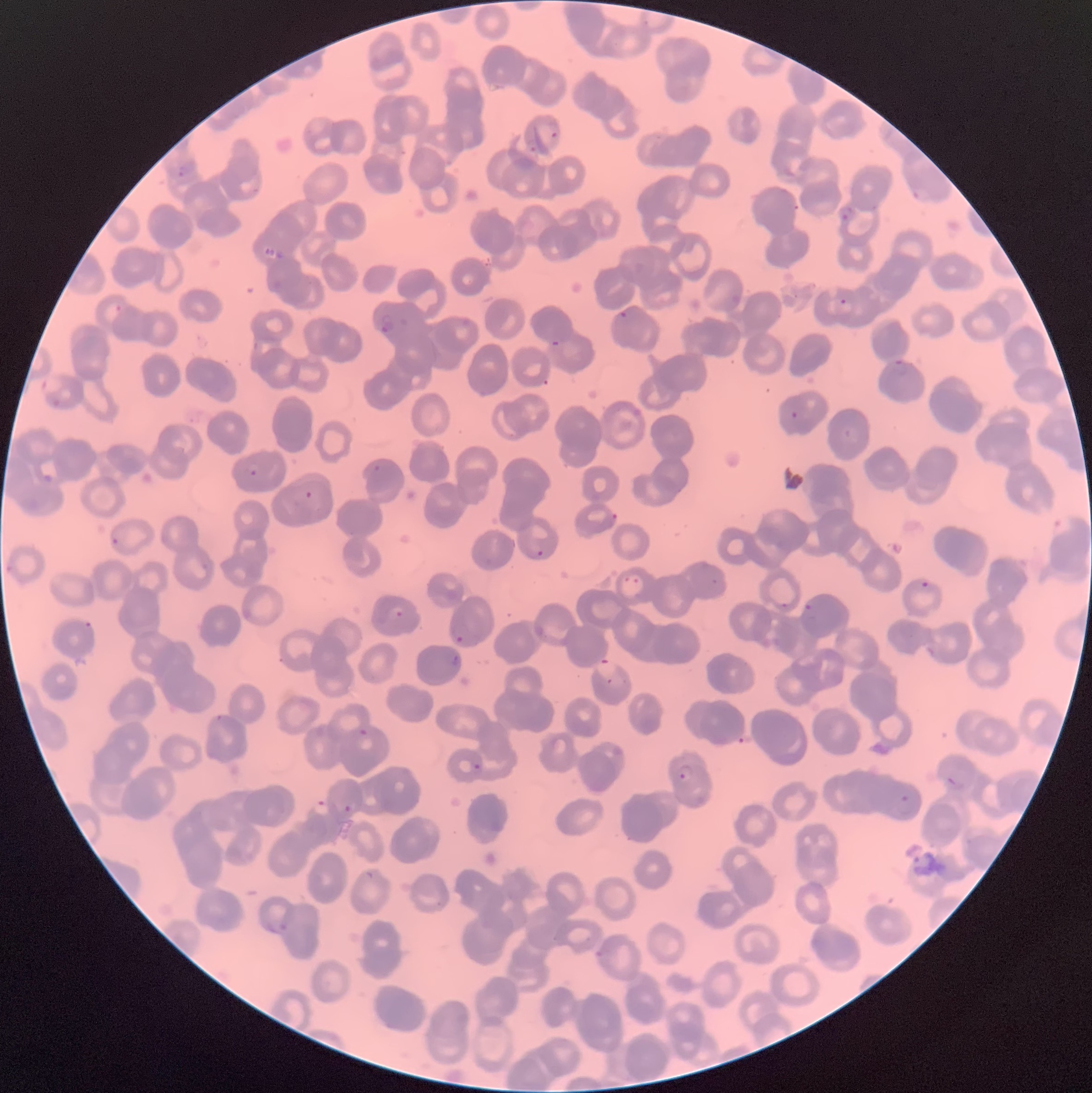
coordinate format = approximate bounding boxes as (x1, y1, x2, y2) in pixels
Plasmodium parasite locations = (545, 121, 561, 138), (527, 138, 537, 152), (178, 160, 197, 177), (913, 185, 933, 202), (840, 205, 854, 221), (838, 298, 847, 306), (617, 311, 628, 321), (380, 312, 396, 333), (552, 340, 561, 347), (893, 359, 908, 375), (41, 376, 64, 393), (53, 399, 61, 406), (790, 411, 799, 419), (247, 461, 261, 476), (373, 464, 381, 471), (43, 475, 54, 483), (305, 490, 313, 500), (111, 524, 129, 546), (536, 550, 545, 558), (623, 571, 645, 593), (921, 579, 930, 588), (804, 603, 812, 611), (387, 606, 404, 618), (454, 631, 465, 643), (453, 653, 461, 671), (597, 658, 618, 678), (607, 678, 629, 686), (359, 728, 370, 738), (473, 762, 482, 773), (679, 763, 697, 782), (948, 777, 956, 787), (898, 795, 914, 816), (313, 800, 330, 816), (344, 804, 352, 812), (363, 869, 375, 880), (265, 919, 289, 933), (595, 950, 605, 958)
Plasmodium parasites too small for a box (approximate centers as (x, y) in pixels) = (784, 604)
modality = light microscopy
red blood cell morphology = rouleaux formation
preparation = thin blood smear
image size = 1092×1093 pixels